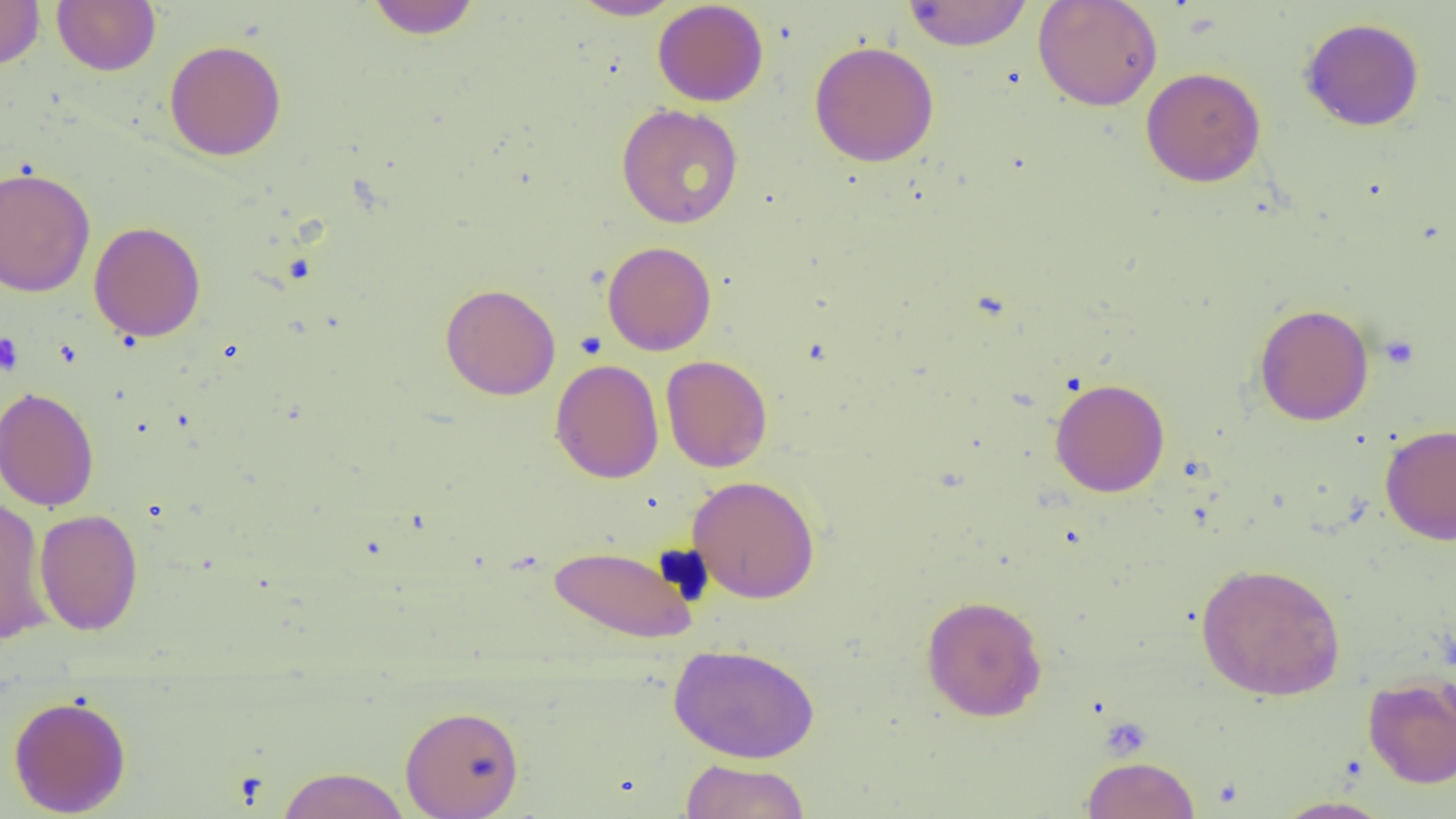
Summary:
  - Coordinate format: approximate bounding boxes as [x1, y1, x2, y2] in pixels
  - Platelet locations: [0, 332, 23, 376], [1379, 334, 1420, 370]
  - Uninfected red blood cell locations: [0, 0, 45, 70], [52, 0, 160, 75], [366, 0, 481, 39], [568, 0, 683, 20], [902, 0, 1033, 51], [1032, 0, 1163, 112], [653, 1, 769, 107], [1299, 17, 1425, 131], [164, 40, 287, 161], [809, 40, 939, 166], [1141, 66, 1266, 187], [616, 103, 744, 229], [0, 166, 96, 297], [89, 221, 206, 342], [602, 241, 716, 356], [440, 283, 560, 399], [1253, 303, 1374, 426], [660, 355, 773, 472], [550, 358, 664, 483], [1049, 377, 1170, 497], [0, 386, 100, 512], [1380, 424, 1456, 545], [687, 475, 820, 604], [0, 496, 54, 646], [35, 508, 144, 636], [549, 544, 698, 644], [1195, 561, 1346, 701], [921, 594, 1048, 722], [668, 643, 820, 763], [1362, 675, 1456, 788], [8, 694, 131, 817], [400, 704, 525, 818], [1081, 756, 1200, 819], [679, 759, 812, 819], [275, 766, 412, 819], [1271, 795, 1396, 819]
  - Slide-level diagnosis: negative for blood parasites
  - Image size: 1456×819 pixels
  - Modality: light microscopy
  - Preparation: thin blood smear
  - Field of view: one of a larger specimen
  - Magnification: 1000x